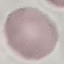
malaria_status: uninfected
image_type: automatically extracted cell patch, resized to 64 × 64 pixels
capture: smartphone through the microscope eyepiece
stain: Giemsa
preparation: thin blood smear